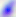

Summary:
  - Identification: Toxoplasma gondii
  - Modality: photomicrograph
  - Magnification: 400x